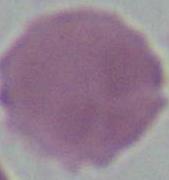

Summary:
  - Magnification: 1000x
  - Modality: micrograph
  - Identification: red blood cell